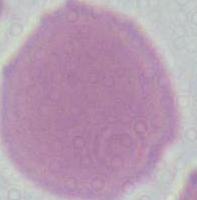

magnification = 1000x
identification = erythrocyte
modality = photomicrograph